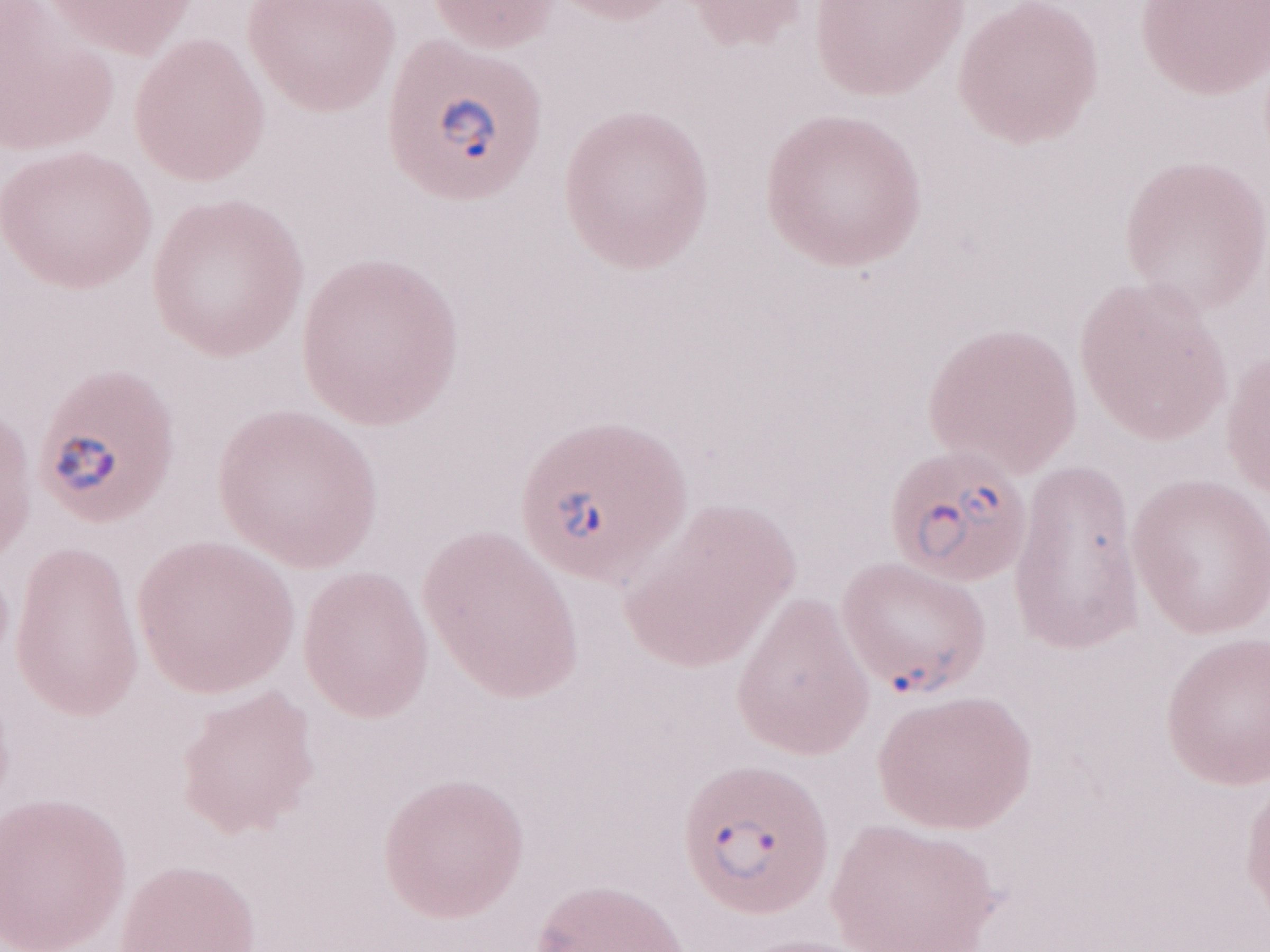
Thin peripheral-blood smear. One field of this slide. May-Grünwald-Giemsa (MGG) stain. Olympus BX43 microscope, Olympus DP73 camera. Malaria diagnosis (patient-level): positive. Magnification: 1,000x. Image is 1270×952 pixels.